Identify the cell.
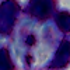
This is a leukocyte.

Micrograph. 1000x magnification.